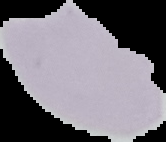
malaria status = uninfected
image type = segmented cell region with the area outside set to black
image size = 166×142 pixels
preparation = thin blood film